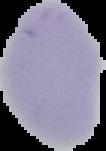
Summary:
  - Image size: 106×151 pixels
  - Malaria status: uninfected
  - Image type: segmented cell region on a black background
  - Preparation: thin blood film